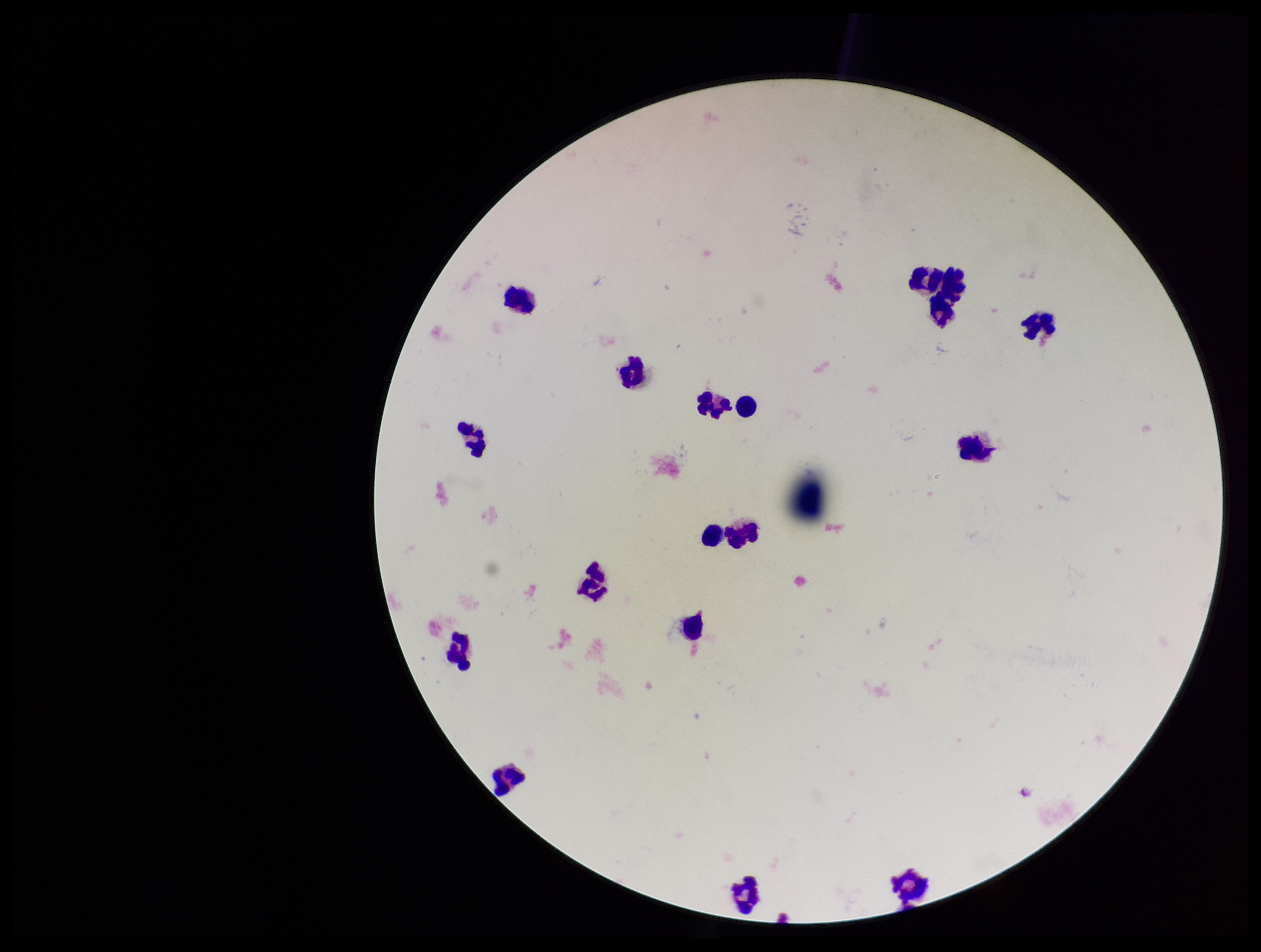
Summary:
  - Preparation: thick smear
  - Plasmodium parasites: none seen
  - Capture: smartphone photograph through the microscope eyepiece
  - Patient malaria status: negative
  - Leukocyte count: 18
  - Image size: 1261×952 pixels
  - Parasite count: 0
  - Stain: Giemsa
  - Field of view: single